Point out every malaria parasite and every leukocyte.
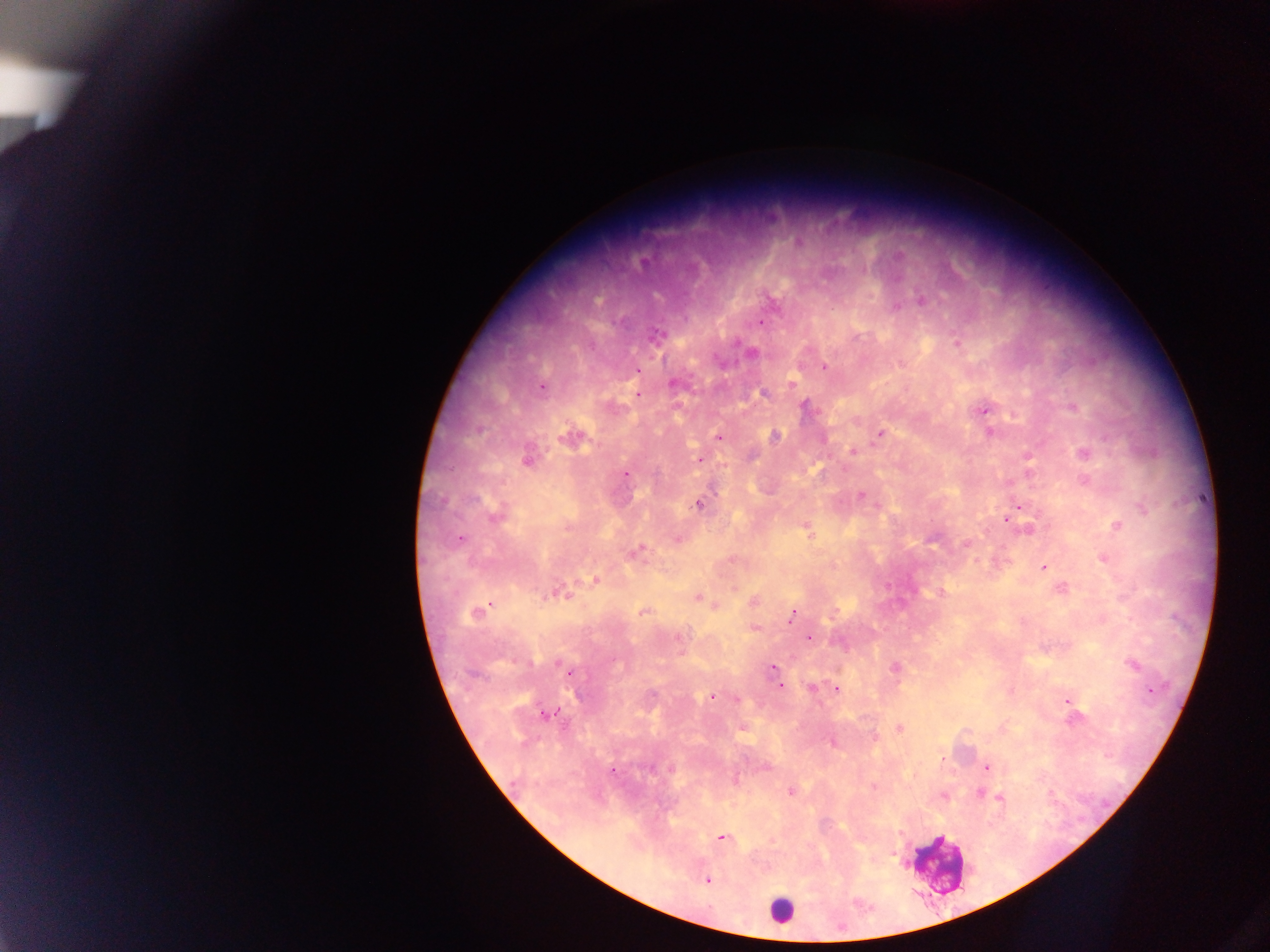

Approximate centers as [x, y] in pixels.
Malaria parasites: [798, 243], [921, 300], [896, 306], [760, 322], [655, 336], [956, 343], [750, 352], [824, 368], [636, 370], [674, 384], [791, 384], [541, 387], [638, 393], [763, 393], [805, 407], [1073, 407], [983, 409], [990, 432], [880, 433], [774, 436], [718, 437], [571, 438], [852, 449], [1082, 454], [1027, 457], [527, 459], [700, 459], [625, 474], [861, 496], [698, 505], [1020, 506], [495, 514], [1005, 518], [1117, 526], [807, 528], [1028, 529], [460, 539], [677, 539], [966, 544], [637, 552], [1103, 557], [1043, 566], [595, 579], [1060, 588], [941, 592], [561, 593], [697, 597], [753, 601], [714, 605], [644, 612], [475, 613], [791, 615], [754, 627], [809, 638], [1132, 664], [774, 668], [895, 668], [780, 687], [812, 688], [837, 688], [1149, 690], [712, 695], [735, 699], [1067, 700], [546, 714], [1002, 727], [899, 728], [832, 742], [986, 767], [765, 768], [612, 771], [873, 787], [790, 792], [979, 792], [943, 796], [999, 796], [720, 837], [707, 880].
Leukocytes: [936, 863], [779, 910].

field of view = single
capture = mobile-phone photograph through a microscope
image size = 1270×952 pixels
preparation = thick blood film
country = Ghana